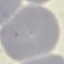
result: negative for malaria parasites
preparation: thin smear
capture: smartphone camera at the microscope eyepiece
image_type: cell patch, automatically extracted from a larger field of view and resized to 64 × 64 pixels
stain: Giemsa